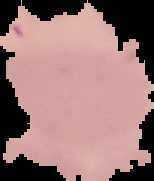

Malaria status: uninfected. From a thin blood film. Image is 154×181 pixels. The area outside the segmented cell region is set to black.